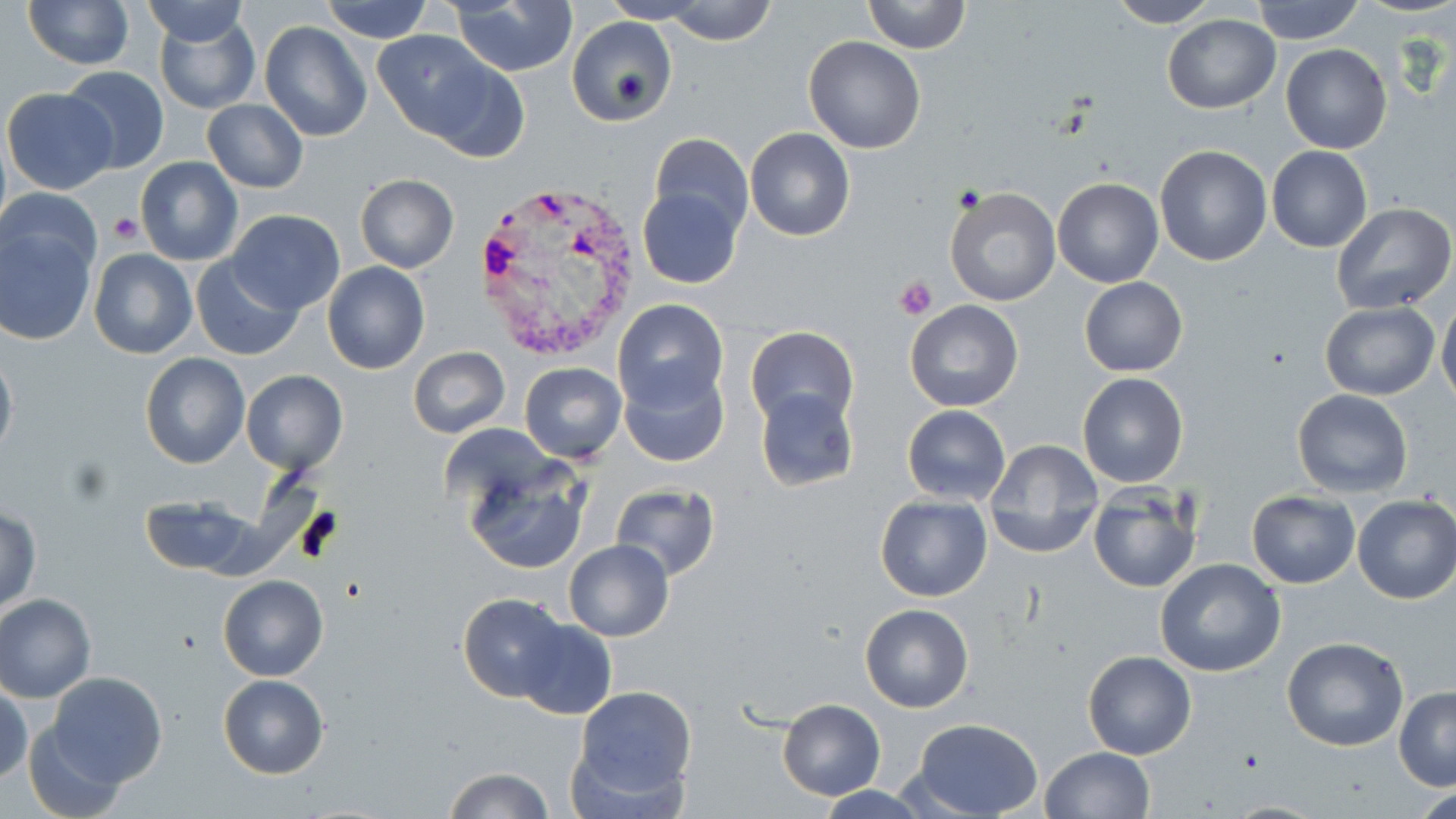
Approximate bounding boxes as (x1,y1)-(x2,y2) corner pairs in pixels. Uninfected red blood cell locations: (138,0)-(252,44), (601,0)-(704,23), (861,0)-(970,54), (1252,0)-(1363,44), (22,1)-(135,71), (321,1)-(433,43), (447,1)-(579,77), (662,1)-(779,46), (1107,1)-(1222,27), (153,12)-(259,113), (1163,13)-(1280,114), (566,17)-(676,125), (259,21)-(374,144), (374,31)-(497,142), (804,36)-(926,154), (1280,43)-(1391,154), (425,61)-(529,161), (61,65)-(170,173), (3,87)-(118,194), (203,100)-(309,194), (745,128)-(855,242), (647,134)-(753,240), (1266,144)-(1373,253), (1154,145)-(1272,265), (135,158)-(243,266), (355,174)-(459,272), (1051,175)-(1164,288), (637,185)-(743,289), (944,186)-(1060,307), (1,187)-(103,283), (1331,202)-(1455,314), (226,209)-(346,314), (0,221)-(97,344), (89,247)-(198,360), (190,254)-(303,361), (323,261)-(429,375), (1079,277)-(1188,377), (1437,292)-(1456,410), (614,299)-(728,411), (905,300)-(1024,412), (1319,302)-(1439,400), (746,326)-(860,432), (407,346)-(510,438), (0,347)-(17,464), (139,353)-(250,470), (519,362)-(627,462), (619,362)-(729,466), (242,371)-(348,476), (1077,373)-(1188,488), (754,387)-(858,492), (1292,388)-(1413,496), (902,405)-(1011,505), (983,438)-(1103,558), (464,461)-(590,575), (609,484)-(721,580), (1088,489)-(1201,594), (1247,491)-(1361,588), (139,495)-(261,578), (874,495)-(992,602), (1351,495)-(1456,605), (1,506)-(41,614), (564,540)-(673,640), (1156,558)-(1287,677), (217,574)-(329,681), (0,593)-(95,702), (458,594)-(571,701), (860,603)-(974,712), (513,619)-(616,721), (1281,637)-(1408,752), (1083,650)-(1197,760), (45,673)-(167,788), (217,674)-(330,778), (0,680)-(30,786), (572,685)-(697,804), (1394,685)-(1456,791), (777,699)-(886,800), (911,718)-(1044,819), (25,720)-(131,818), (1040,747)-(1156,819), (442,768)-(555,818). Platelet locations: (953,184)-(985,212), (107,212)-(145,245), (893,275)-(937,321). Plasmodium vivax-infected red blood cell locations: (473,184)-(647,360). Slide-level diagnosis: Plasmodium vivax. One field of a larger specimen. Optical microscopy. Thin blood film. May-Grünwald-Giemsa stain. Image is 1456×819 pixels. 1000x magnification.